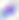
modality = photomicrograph
identification = Toxoplasma gondii
magnification = 400x